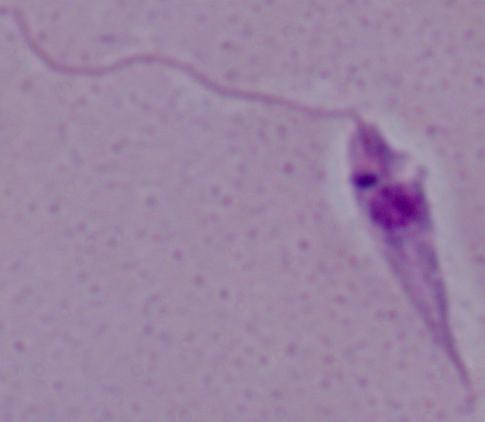

Micrograph. Captured at 1000x magnification. A Leishmania parasite is shown.